Give the position of every leukocyte visible.
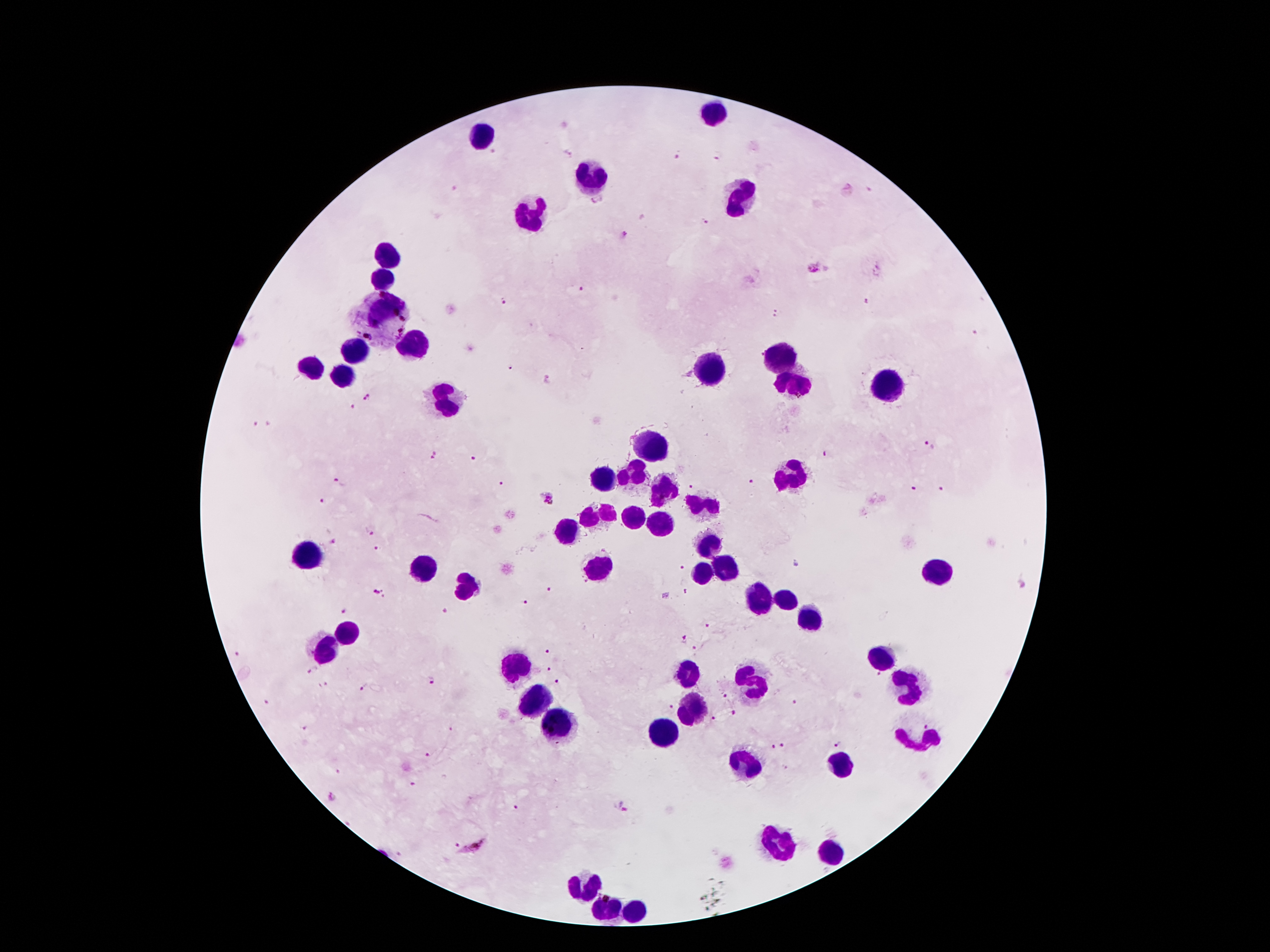

Approximate object centers, in pixels from the top-left corner.
Leukocytes: (x=719, y=115), (x=484, y=136), (x=595, y=181), (x=742, y=202), (x=528, y=214), (x=389, y=252), (x=387, y=277), (x=387, y=315), (x=412, y=346), (x=351, y=353), (x=782, y=359), (x=305, y=367), (x=711, y=369), (x=345, y=376), (x=795, y=380), (x=887, y=384), (x=446, y=401), (x=650, y=441), (x=635, y=472), (x=599, y=479), (x=792, y=479), (x=664, y=491), (x=702, y=504), (x=599, y=516), (x=635, y=518), (x=660, y=525), (x=568, y=533), (x=711, y=552), (x=311, y=560), (x=429, y=568), (x=601, y=569), (x=725, y=569), (x=937, y=571), (x=704, y=575), (x=468, y=588), (x=784, y=596), (x=757, y=605), (x=809, y=617), (x=347, y=632), (x=328, y=649), (x=516, y=669), (x=689, y=677), (x=759, y=681), (x=535, y=703), (x=690, y=708), (x=555, y=728), (x=655, y=733), (x=841, y=763), (x=740, y=767), (x=780, y=842), (x=832, y=851), (x=583, y=890), (x=631, y=910), (x=606, y=912).

Summary:
  - Malaria parasite locations: (x=718, y=154), (x=678, y=155), (x=597, y=200), (x=706, y=222), (x=624, y=236), (x=813, y=266), (x=584, y=289), (x=865, y=299), (x=502, y=302), (x=775, y=312), (x=973, y=333), (x=513, y=368), (x=547, y=380), (x=368, y=397), (x=351, y=406), (x=253, y=423), (x=929, y=444), (x=826, y=453), (x=434, y=455), (x=473, y=458), (x=753, y=480), (x=339, y=482), (x=500, y=483), (x=692, y=484), (x=913, y=487), (x=941, y=490), (x=549, y=497), (x=322, y=500), (x=371, y=532), (x=335, y=542), (x=376, y=549), (x=682, y=568), (x=1023, y=585), (x=548, y=588), (x=379, y=591), (x=684, y=592), (x=525, y=602), (x=443, y=610), (x=344, y=612), (x=708, y=627), (x=685, y=639), (x=694, y=649), (x=546, y=651), (x=239, y=653), (x=313, y=668), (x=550, y=670), (x=879, y=676), (x=433, y=680), (x=557, y=683), (x=324, y=686), (x=363, y=688), (x=725, y=696), (x=794, y=702), (x=264, y=703), (x=672, y=708), (x=733, y=713), (x=716, y=717), (x=305, y=728), (x=449, y=728), (x=837, y=745), (x=773, y=747), (x=784, y=747), (x=427, y=755), (x=414, y=785), (x=333, y=799), (x=621, y=806), (x=515, y=808), (x=457, y=845), (x=476, y=848)
  - Magnification: 100x
  - Stain: Giemsa
  - Patient malaria status: infected with Plasmodium falciparum
  - Capture: smartphone camera through the microscope eyepiece
  - Image size: 1270×952 pixels
  - Field of view: one from this slide
  - Preparation: thick blood smear